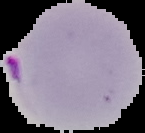
image size = 145×133 pixels
result = malaria parasites detected
preparation = thin blood film
image type = cell region segmented out of the field of view; surrounding area masked to black